State the blood parasite species.
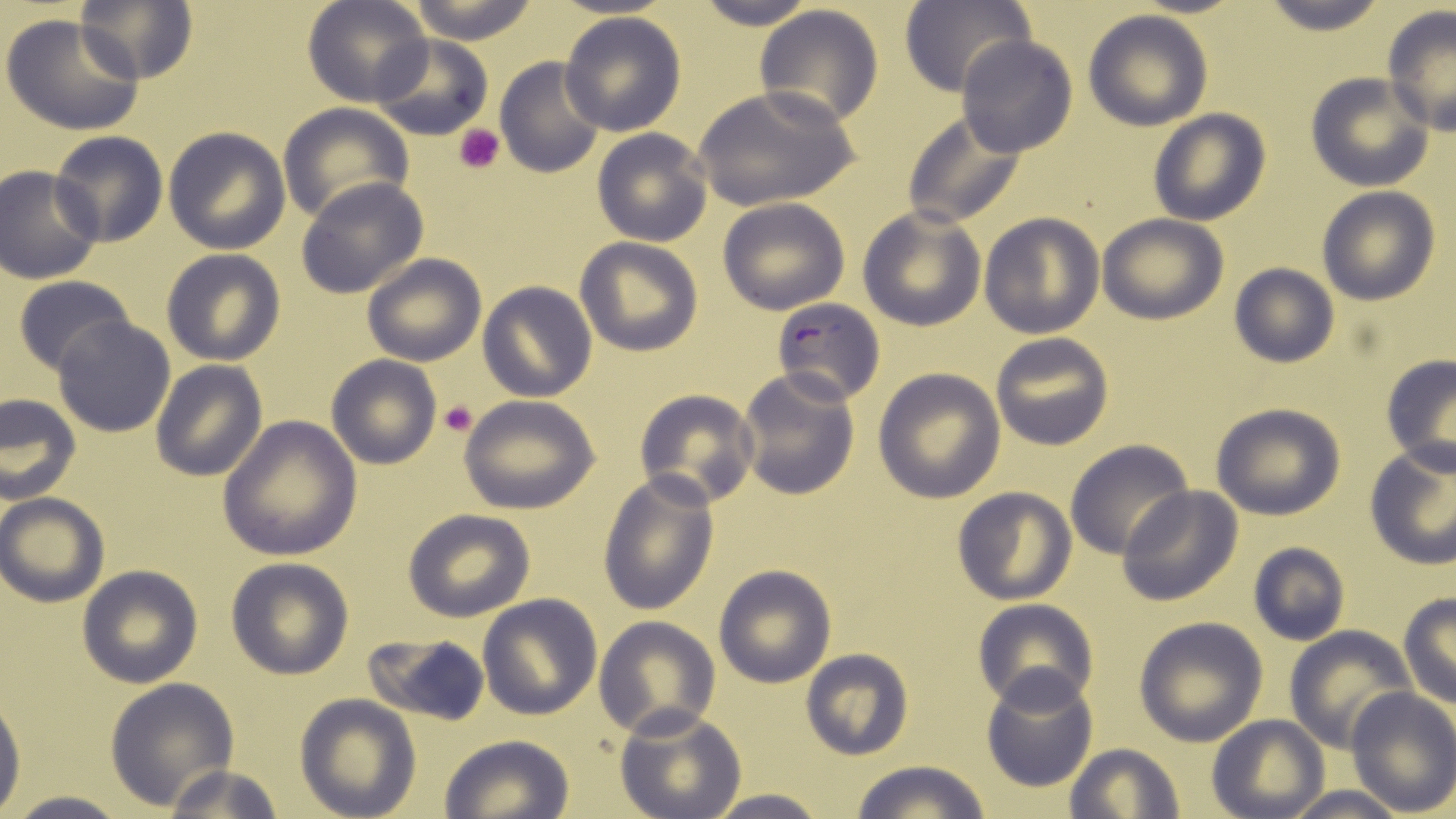
Plasmodium falciparum.

{
  "image_size": "1456×819 pixels",
  "stain": "May-Grünwald-Giemsa",
  "preparation": "thin blood smear",
  "modality": "optical microscopy",
  "uninfected_red_blood_cell_locations": "approximate bounding boxes as (x1, y1, x2, y2) in pixels: (74, 0, 198, 85), (303, 0, 432, 109), (406, 0, 544, 43), (686, 0, 824, 29), (1257, 0, 1388, 35), (901, 2, 1031, 98), (752, 4, 885, 130), (1380, 6, 1455, 135), (1084, 10, 1213, 131), (558, 11, 688, 137), (1, 12, 145, 137), (955, 34, 1077, 158), (370, 35, 493, 141), (495, 55, 609, 179), (1305, 73, 1435, 191), (694, 86, 859, 212), (279, 103, 413, 226), (904, 109, 1028, 229), (1148, 109, 1271, 226), (163, 126, 291, 254), (591, 128, 713, 246), (50, 130, 168, 248), (1, 166, 102, 284), (297, 177, 429, 300), (1316, 186, 1441, 306), (718, 198, 851, 315), (858, 206, 987, 332), (979, 212, 1105, 339), (1097, 213, 1229, 325), (575, 237, 702, 356), (162, 249, 286, 366), (361, 253, 486, 367), (1228, 264, 1339, 368), (13, 275, 137, 378), (478, 282, 597, 402), (52, 315, 178, 438), (989, 333, 1114, 451), (326, 355, 442, 469), (1380, 357, 1456, 475), (150, 361, 267, 480), (873, 367, 1006, 503), (734, 368, 860, 502), (634, 389, 760, 508), (0, 392, 81, 502), (459, 395, 601, 513), (1210, 401, 1346, 520), (218, 416, 362, 560), (1064, 439, 1194, 560), (1363, 440, 1456, 568), (596, 468, 720, 618), (1118, 486, 1242, 607), (950, 487, 1077, 605), (1, 493, 110, 607), (403, 509, 536, 622), (1246, 541, 1350, 648), (226, 557, 355, 679), (76, 564, 203, 689), (713, 564, 837, 688), (477, 594, 603, 721), (1398, 594, 1456, 710), (972, 599, 1098, 712), (594, 617, 721, 739), (1133, 617, 1268, 746), (1285, 625, 1415, 752), (364, 634, 489, 725), (799, 648, 913, 762), (980, 667, 1098, 791), (103, 677, 239, 811), (1345, 687, 1456, 815), (0, 689, 24, 810), (295, 693, 421, 819), (615, 706, 747, 819), (1207, 715, 1328, 818), (438, 734, 574, 819), (1064, 743, 1185, 819), (848, 760, 995, 818), (160, 763, 288, 818), (1283, 784, 1406, 819), (697, 789, 831, 819), (2, 792, 134, 819)",
  "field_of_view": "one of a larger specimen",
  "magnification": "1000x",
  "platelet_locations": "approximate bounding boxes as (x1, y1, x2, y2) in pixels: (453, 124, 504, 174), (439, 401, 478, 437)",
  "plasmodium_falciparum_infected_red_blood_cell_locations": "approximate bounding boxes as (x1, y1, x2, y2) in pixels: (770, 297, 885, 406)"
}